Name the parasite shown.
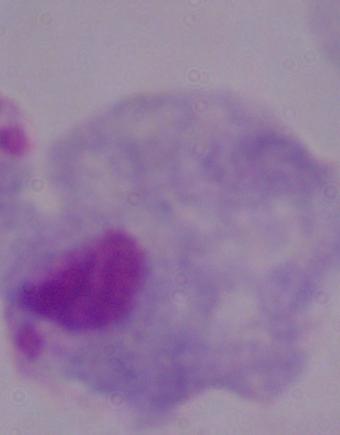

This is a trichomonad.

modality: micrograph
magnification: 1000x